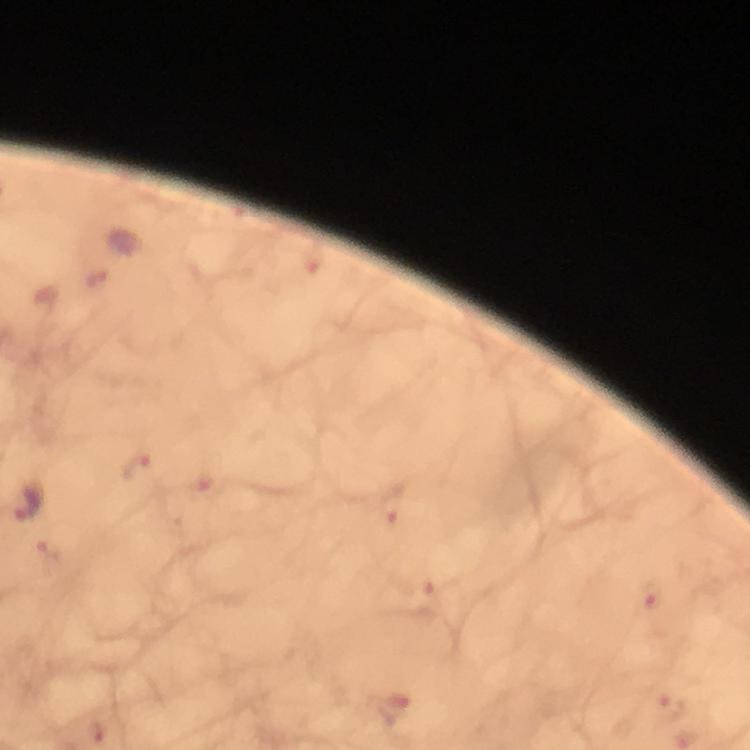

capture = smartphone mounted on the microscope
preparation = thick blood film
stain = Giemsa
context = from a malaria diagnostic workup
image size = 750×750 pixels
cropped from = a single field of view
magnification = 100x
immersion oil = applied
malaria parasite locations = approximate centers as {x, y} in pixels: {96, 278}, {137, 467}, {28, 504}, {392, 504}, {50, 552}, {432, 591}, {653, 604}, {671, 708}, {394, 711}